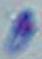

Summary:
  - Magnification: 1000x
  - Modality: photomicrograph
  - Identification: Toxoplasma gondii